Locate every blood parasite and identify its species.
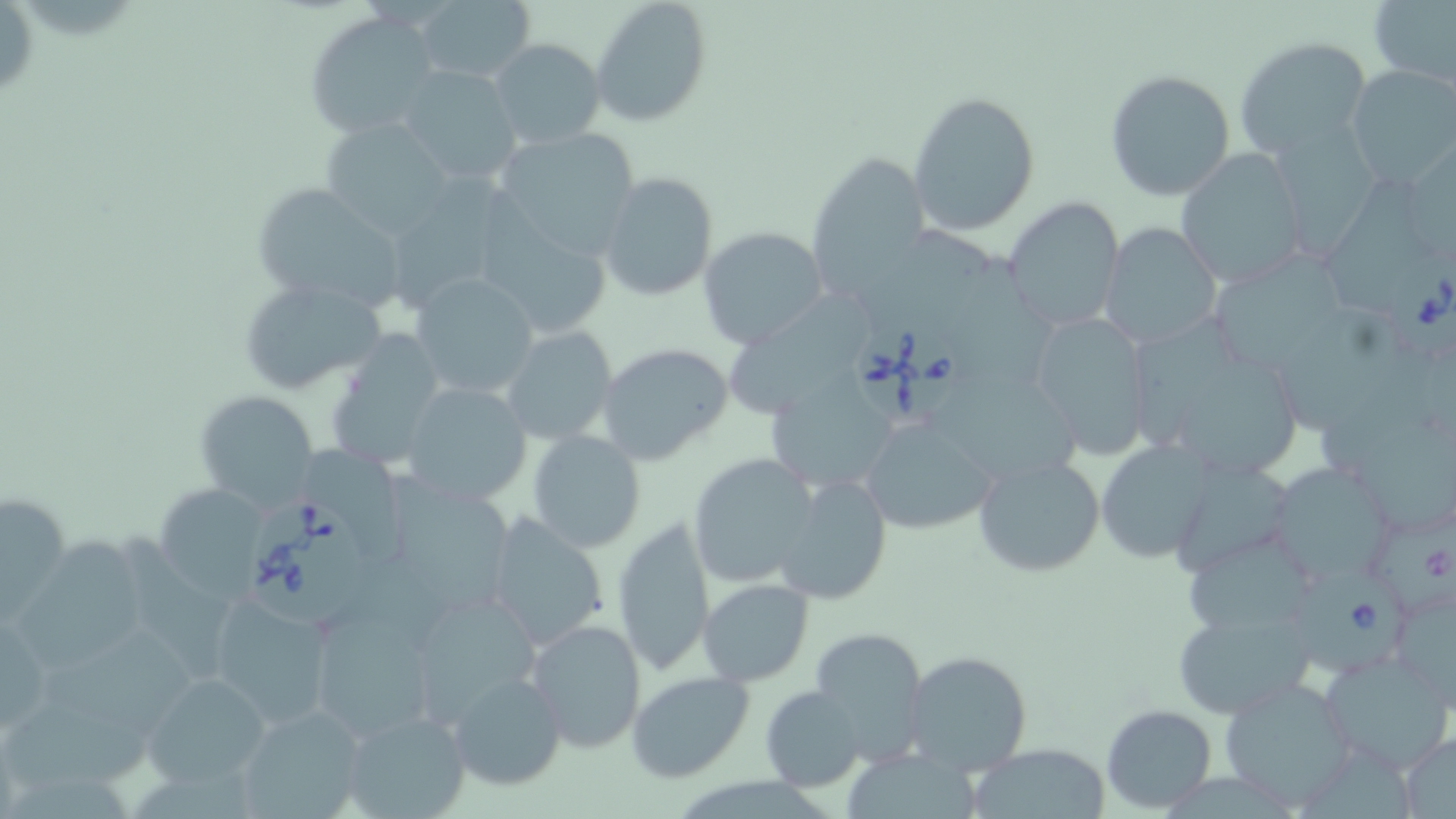

Approximate bounding boxes as named x1/y1/x2/y2 corners in pixels.
Babesia divergens-infected red blood cells: (x1=1392, y1=252, x2=1456, y2=362), (x1=857, y1=323, x2=968, y2=420), (x1=245, y1=499, x2=370, y2=630), (x1=1299, y1=567, x2=1409, y2=677).
No Plasmodium falciparum, Plasmodium ovale, Plasmodium malariae, Plasmodium vivax, or Trypanosoma brucei observed.

Uninfected red blood cell locations: (x1=0, y1=0, x2=37, y2=89), (x1=27, y1=0, x2=129, y2=41), (x1=590, y1=0, x2=711, y2=126), (x1=1369, y1=0, x2=1456, y2=90), (x1=408, y1=2, x2=537, y2=85), (x1=304, y1=9, x2=442, y2=138), (x1=1234, y1=35, x2=1371, y2=157), (x1=488, y1=38, x2=606, y2=150), (x1=1347, y1=65, x2=1455, y2=186), (x1=397, y1=66, x2=524, y2=188), (x1=1104, y1=68, x2=1237, y2=200), (x1=907, y1=89, x2=1041, y2=236), (x1=319, y1=118, x2=458, y2=239), (x1=490, y1=127, x2=641, y2=265), (x1=807, y1=149, x2=929, y2=298), (x1=1178, y1=150, x2=1311, y2=288), (x1=1270, y1=150, x2=1387, y2=264), (x1=599, y1=172, x2=717, y2=301), (x1=383, y1=177, x2=525, y2=313), (x1=1317, y1=177, x2=1438, y2=320), (x1=249, y1=180, x2=411, y2=313), (x1=1002, y1=196, x2=1126, y2=332), (x1=470, y1=212, x2=615, y2=341), (x1=862, y1=219, x2=998, y2=349), (x1=1099, y1=223, x2=1222, y2=348), (x1=697, y1=226, x2=828, y2=349), (x1=952, y1=255, x2=1066, y2=392), (x1=1213, y1=260, x2=1349, y2=364), (x1=410, y1=273, x2=541, y2=400), (x1=238, y1=277, x2=389, y2=395), (x1=734, y1=295, x2=875, y2=421), (x1=1282, y1=305, x2=1434, y2=447), (x1=1132, y1=310, x2=1256, y2=449), (x1=1027, y1=311, x2=1152, y2=458), (x1=501, y1=325, x2=619, y2=447), (x1=324, y1=330, x2=451, y2=470), (x1=596, y1=342, x2=734, y2=466), (x1=1180, y1=361, x2=1311, y2=487), (x1=1322, y1=364, x2=1456, y2=481), (x1=939, y1=372, x2=1085, y2=489), (x1=400, y1=379, x2=535, y2=506), (x1=766, y1=380, x2=892, y2=492), (x1=195, y1=390, x2=319, y2=511), (x1=860, y1=420, x2=995, y2=532), (x1=528, y1=430, x2=646, y2=553), (x1=1094, y1=441, x2=1211, y2=563), (x1=309, y1=445, x2=407, y2=562), (x1=688, y1=452, x2=819, y2=589), (x1=973, y1=453, x2=1105, y2=578), (x1=1170, y1=463, x2=1294, y2=575), (x1=389, y1=465, x2=511, y2=615), (x1=1276, y1=470, x2=1400, y2=582), (x1=771, y1=474, x2=893, y2=606), (x1=153, y1=484, x2=271, y2=601), (x1=1, y1=490, x2=71, y2=618), (x1=1378, y1=506, x2=1456, y2=612), (x1=483, y1=512, x2=612, y2=653), (x1=614, y1=516, x2=714, y2=676), (x1=21, y1=531, x2=140, y2=672), (x1=122, y1=532, x2=235, y2=683), (x1=1189, y1=534, x2=1321, y2=633), (x1=698, y1=578, x2=814, y2=686), (x1=208, y1=594, x2=335, y2=727), (x1=1401, y1=597, x2=1456, y2=719), (x1=423, y1=599, x2=539, y2=728), (x1=1172, y1=605, x2=1316, y2=719), (x1=306, y1=606, x2=442, y2=746), (x1=0, y1=608, x2=56, y2=744), (x1=525, y1=617, x2=648, y2=754), (x1=47, y1=618, x2=204, y2=737), (x1=809, y1=627, x2=929, y2=760), (x1=903, y1=649, x2=1035, y2=779), (x1=1321, y1=650, x2=1455, y2=774), (x1=625, y1=670, x2=754, y2=783), (x1=446, y1=671, x2=567, y2=791), (x1=142, y1=672, x2=272, y2=787), (x1=1218, y1=677, x2=1359, y2=810), (x1=759, y1=685, x2=867, y2=792), (x1=1, y1=703, x2=148, y2=791), (x1=235, y1=704, x2=368, y2=819), (x1=1100, y1=704, x2=1218, y2=812), (x1=338, y1=708, x2=473, y2=819), (x1=1395, y1=731, x2=1456, y2=817), (x1=968, y1=742, x2=1111, y2=818), (x1=1297, y1=746, x2=1416, y2=819), (x1=847, y1=751, x2=987, y2=819), (x1=135, y1=768, x2=254, y2=818), (x1=685, y1=772, x2=831, y2=818), (x1=1168, y1=772, x2=1297, y2=819), (x1=3, y1=773, x2=146, y2=819). Slide-level diagnosis: Babesia divergens. May-Grünwald-Giemsa stain. Thin blood smear. Light microscopy. One field of a larger specimen. Image is 1456×819 pixels. Captured at 1000x magnification.